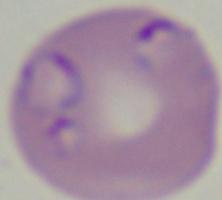
{
  "magnification": "1000x",
  "modality": "photomicrograph",
  "identification": "Babesia"
}